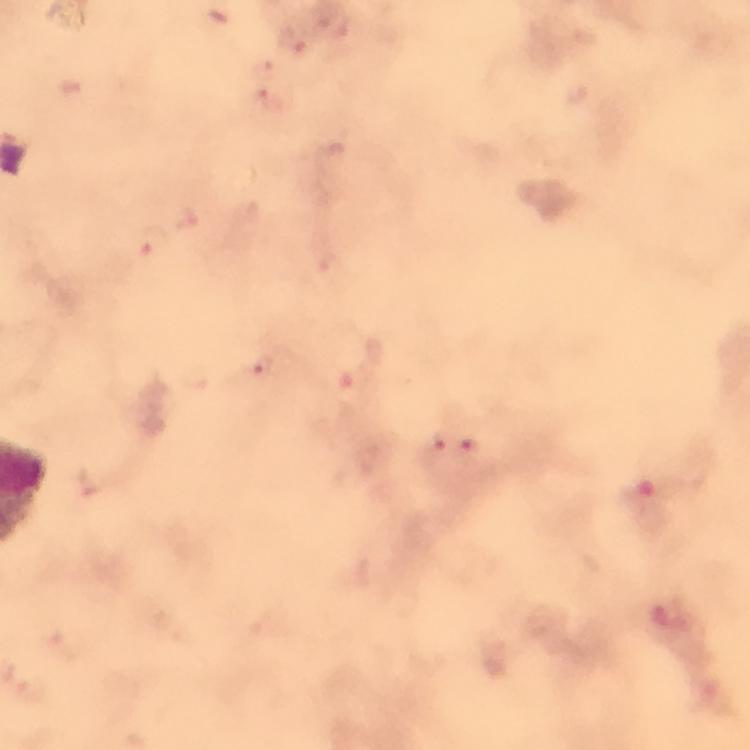
capture = smartphone photograph through a microscope
image size = 750×750 pixels
preparation = thick blood film
context = from a malaria diagnostic workup
stain = Giemsa
magnification = 100x
cropped from = one field of view
Plasmodium parasite locations = approximate object centers, in pixels from the top-left corner: (x=293, y=41), (x=153, y=241), (x=263, y=363), (x=441, y=442), (x=468, y=447)
immersion oil = applied